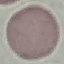

Summary:
  - Malaria status: uninfected
  - Stain: Giemsa
  - Capture: smartphone camera at the microscope eyepiece
  - Image type: automatically extracted cell patch, resized to 64 × 64 pixels
  - Preparation: thin blood smear